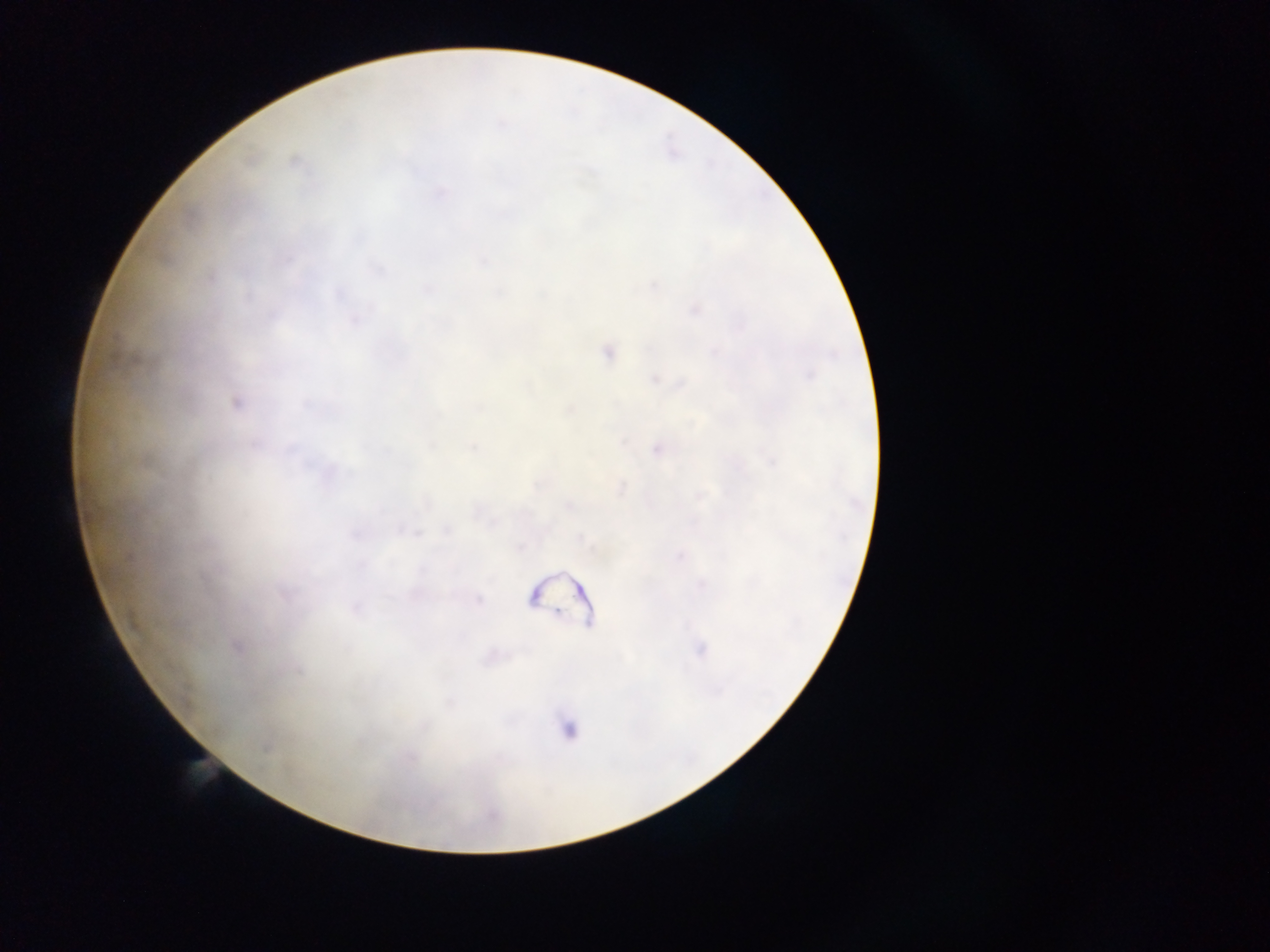
Approximate centers as (x, y) in pixels.
Summary:
  - Plasmodium parasite locations: (294, 161), (693, 309), (607, 352), (656, 377), (236, 401), (658, 448), (566, 505), (478, 598), (354, 607), (236, 646), (699, 650)
  - Preparation: thick blood smear
  - Image size: 1270×952 pixels
  - Field of view: single
  - Capture: mobile-phone photograph through a microscope
  - Country: Ghana